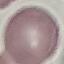
Summary:
  - Malaria status: uninfected
  - Stain: Giemsa
  - Capture: smartphone camera at the microscope eyepiece
  - Preparation: thin smear
  - Image type: automatically extracted cell patch, resized to 64 × 64 pixels